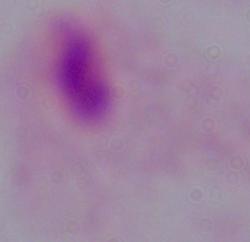
modality = photomicrograph
identification = trichomonad
magnification = 1000x